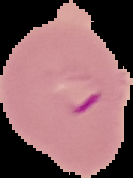

{
  "result": "Plasmodium parasites identified",
  "image_type": "cell region segmented out of the field of view; surrounding area masked to black",
  "image_size": "133×178 pixels",
  "preparation": "thin blood film"
}